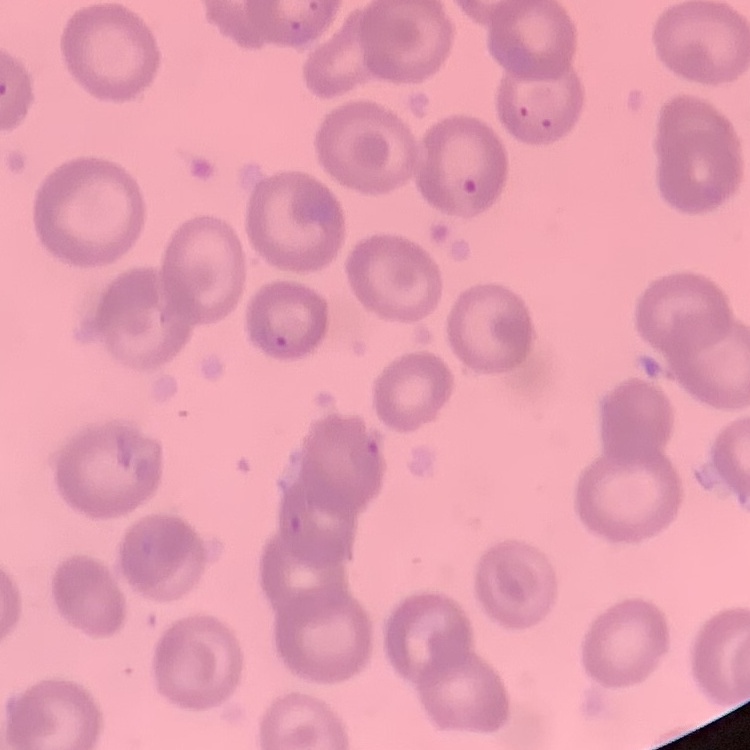
The red blood cells show no rouleaux formation. Stained with either Field's or Giemsa. One tile cut from a larger photomicrograph. Thin peripheral smear.